Assess the morphology of the erythrocytes.
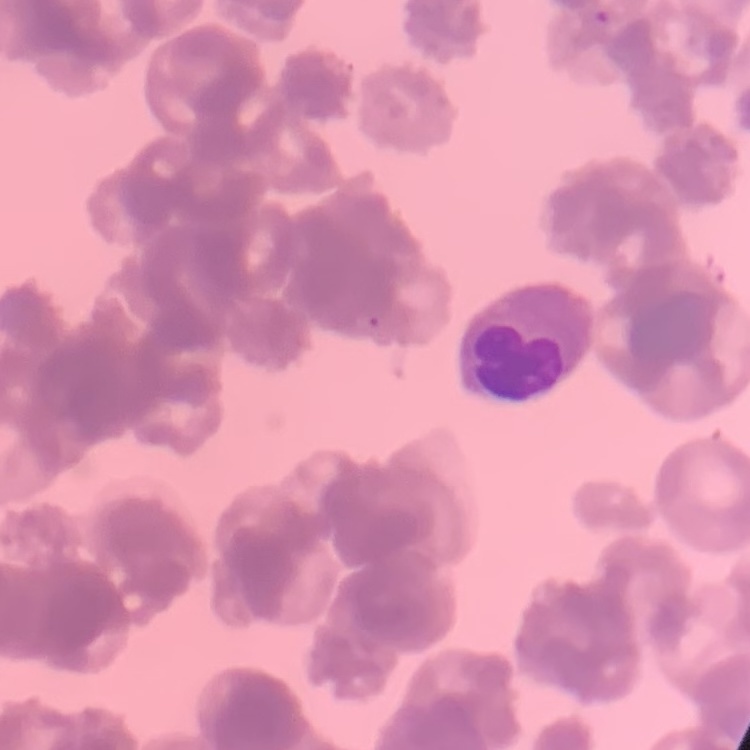
They show rouleaux formation.

Thin blood smear. One tile cut from a larger photomicrograph. Stained with either Field's or Giemsa.